Give the extent of all Plasmodium ovale-infected red blood cells.
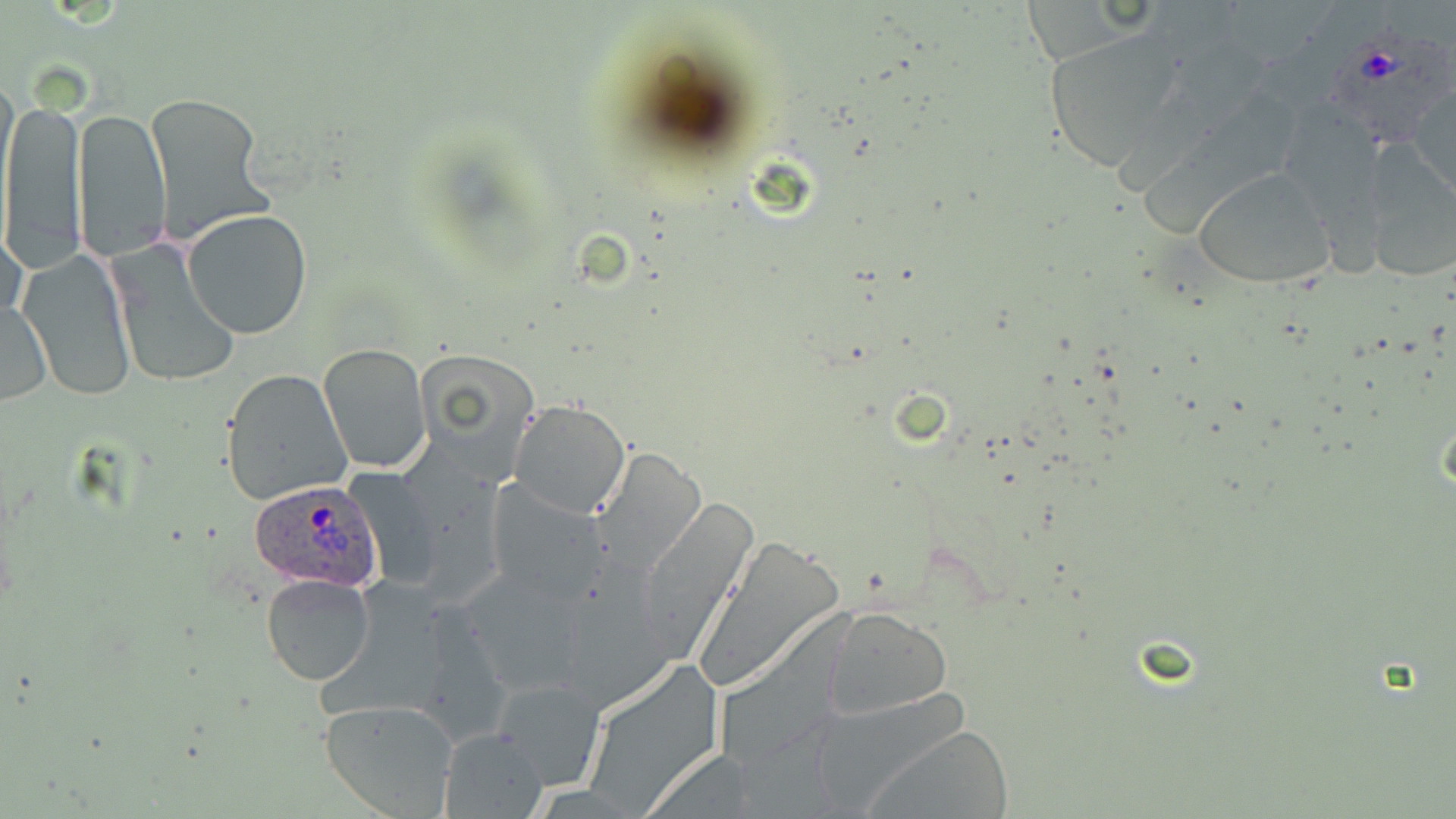
Approximate bounding boxes as (x1,y1)-(x2,y2) corner pairs in pixels.
Plasmodium ovale-infected red blood cells: (1330,35)-(1451,147), (248,481)-(384,591).

{
  "slide_level_diagnosis": "Plasmodium ovale",
  "stain": "May-Grünwald-Giemsa",
  "preparation": "thin blood film",
  "magnification": "1000x",
  "modality": "optical microscopy",
  "image_size": "1456×819 pixels",
  "uninfected_red_blood_cell_locations": "approximate bounding boxes as (x1,y1)-(x2,y2) corner pairs in pixels: (1019,1)-(1131,63), (1043,31)-(1184,169), (0,73)-(18,196), (1409,84)-(1455,199), (143,91)-(274,241), (2,96)-(83,272), (1272,98)-(1384,212), (74,105)-(172,261), (1357,149)-(1456,282), (1190,166)-(1338,291), (183,209)-(313,339), (1,220)-(28,336), (107,241)-(240,388), (18,247)-(136,400), (0,300)-(52,404), (317,344)-(431,472), (415,349)-(542,481), (221,369)-(352,508), (507,399)-(632,519), (592,447)-(707,575), (486,479)-(610,602), (635,496)-(763,660), (694,535)-(842,689), (461,566)-(593,698), (260,574)-(376,687), (825,608)-(951,720), (492,677)-(606,792), (318,699)-(460,819), (861,723)-(1017,817), (439,726)-(547,817)",
  "field_of_view": "one of a larger specimen"
}